Assess this cell for malaria.
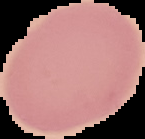

Uninfected.

Segmented cell region on a black background. Image is 145×139 pixels. From a thin blood film.